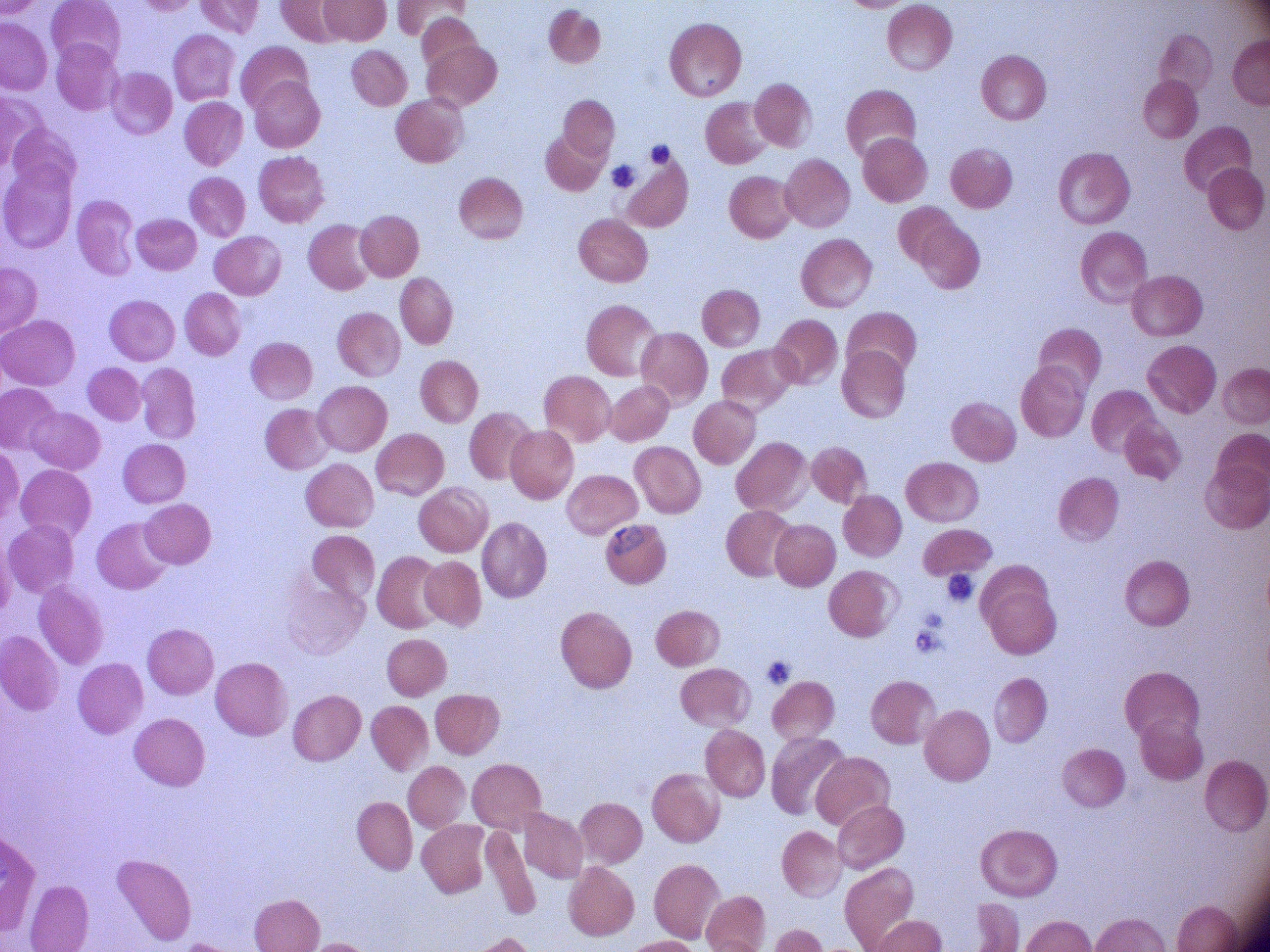

Approximate bounding boxes as (x1,y1)-(x2,y2) corner pairs in pixels, from the source annotation, which is not necessarily exhaustive.
Summary:
  - Trophozoite locations: (600,517)-(653,562)
  - Microscope: Leica DM2000 with built-in camera
  - Stain: Giemsa
  - Image size: 1270×952 pixels
  - Species: Plasmodium falciparum
  - Preparation: thin blood film
  - Magnification: 100x
  - Field of view: one from this slide